Identify the parasite.
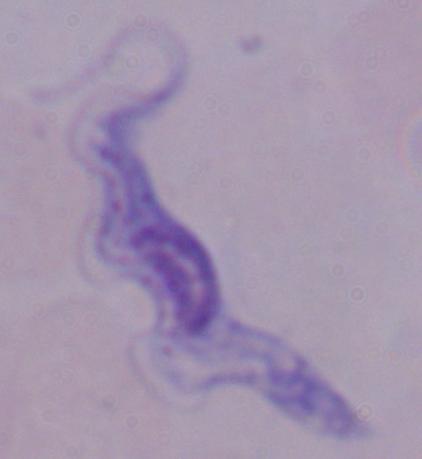

This is a trypanosome.

Summary:
  - Modality: micrograph
  - Magnification: 1000x